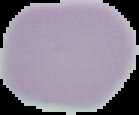

preparation = thin blood smear
result = no malaria parasites detected
image type = segmented cell region on a black background
image size = 139×115 pixels